Comment on the morphology of the red blood cells.
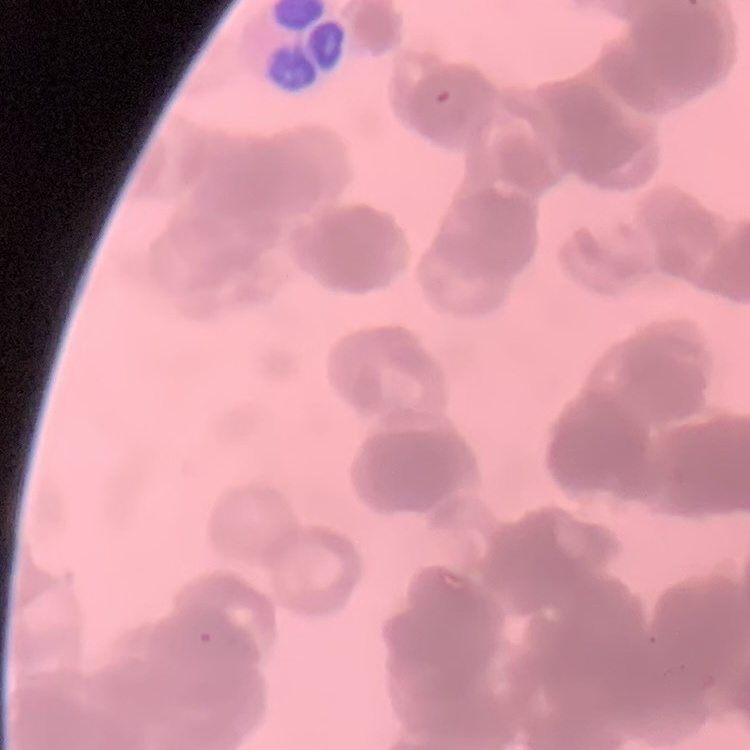
Rouleaux formation.

Summary:
  - Stain: Field's or Giemsa
  - Preparation: thin blood smear
  - Image type: one tile cut from a larger photomicrograph